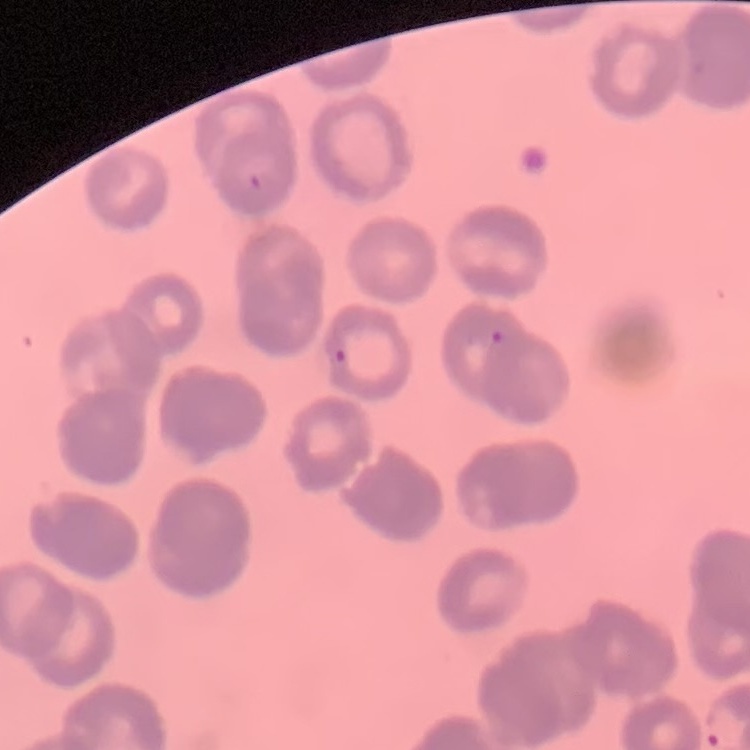
erythrocyte morphology = rouleaux formation
stain = Field's or Giemsa
image type = square crop of a larger photomicrograph
preparation = thin blood film